Classify this cell by malaria status.
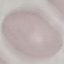

It is uninfected.

Summary:
  - Preparation: thin blood smear
  - Stain: Giemsa
  - Capture: smartphone camera at the microscope eyepiece
  - Image type: automatically extracted cell patch, resized to 64 × 64 pixels